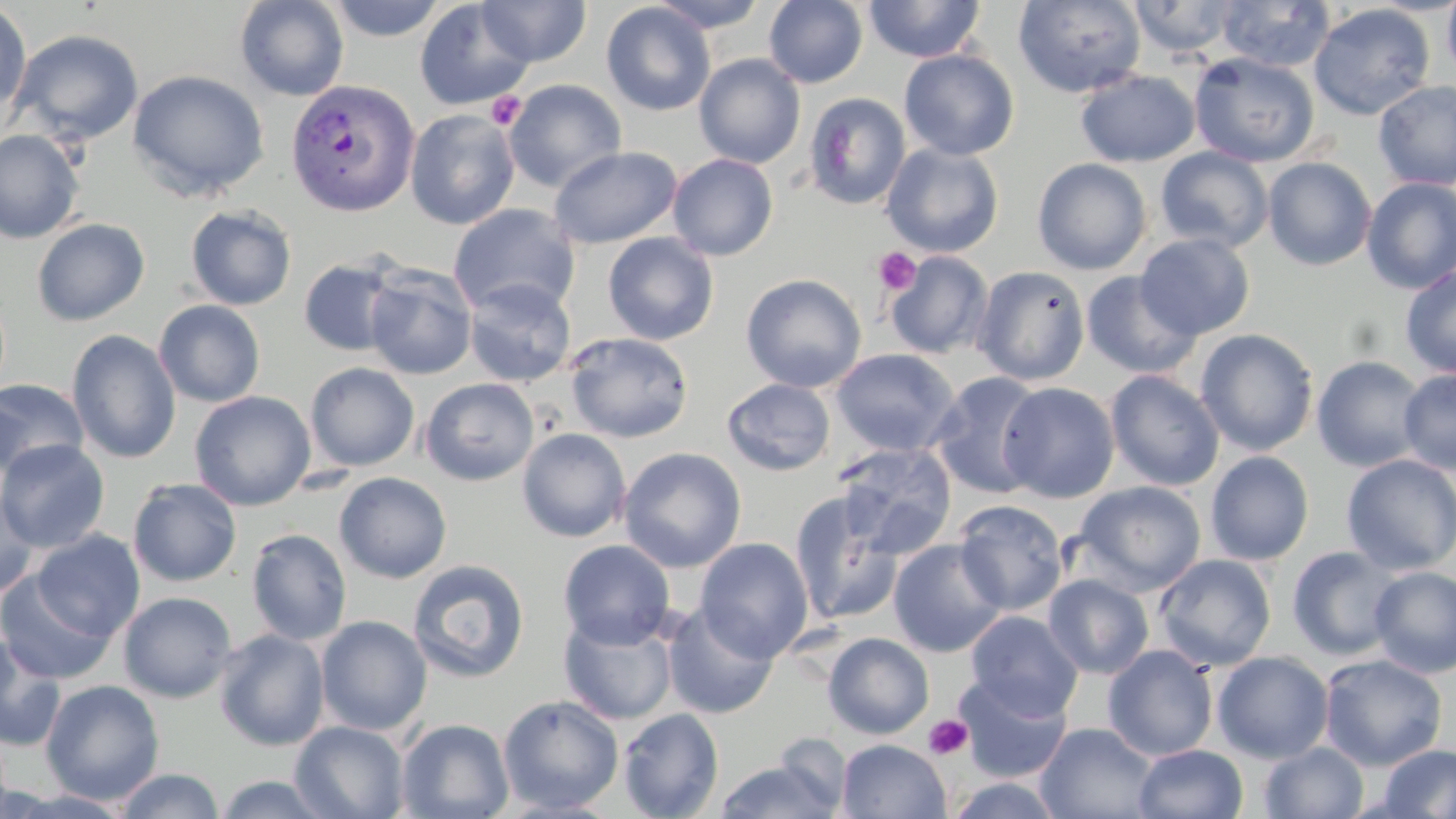 Approximate bounding boxes as named x1/y1/x2/y2 corners in pixels. Uninfected red blood cell locations: (x1=235, y1=0, x2=349, y2=101), (x1=326, y1=0, x2=448, y2=41), (x1=648, y1=0, x2=770, y2=33), (x1=763, y1=0, x2=868, y2=88), (x1=864, y1=0, x2=985, y2=63), (x1=1013, y1=0, x2=1146, y2=98), (x1=1128, y1=0, x2=1242, y2=57), (x1=1441, y1=0, x2=1456, y2=83), (x1=414, y1=1, x2=534, y2=110), (x1=476, y1=1, x2=591, y2=67), (x1=1214, y1=1, x2=1336, y2=72), (x1=601, y1=2, x2=716, y2=116), (x1=0, y1=3, x2=32, y2=119), (x1=1308, y1=4, x2=1435, y2=121), (x1=10, y1=29, x2=144, y2=146), (x1=899, y1=49, x2=1020, y2=160), (x1=1189, y1=52, x2=1320, y2=168), (x1=694, y1=53, x2=806, y2=169), (x1=127, y1=68, x2=270, y2=201), (x1=1075, y1=69, x2=1200, y2=167), (x1=503, y1=79, x2=627, y2=191), (x1=1373, y1=80, x2=1456, y2=190), (x1=804, y1=93, x2=912, y2=210), (x1=405, y1=108, x2=520, y2=230), (x1=0, y1=129, x2=85, y2=244), (x1=880, y1=143, x2=1005, y2=257), (x1=550, y1=145, x2=683, y2=249), (x1=1155, y1=146, x2=1274, y2=253), (x1=668, y1=153, x2=779, y2=260), (x1=1032, y1=157, x2=1152, y2=275), (x1=1262, y1=157, x2=1377, y2=270), (x1=1360, y1=177, x2=1456, y2=294), (x1=448, y1=203, x2=580, y2=318), (x1=185, y1=205, x2=297, y2=310), (x1=31, y1=218, x2=150, y2=326), (x1=602, y1=232, x2=719, y2=345), (x1=1135, y1=232, x2=1256, y2=340), (x1=884, y1=250, x2=993, y2=359), (x1=298, y1=258, x2=403, y2=356), (x1=1400, y1=264, x2=1456, y2=378), (x1=364, y1=265, x2=477, y2=379), (x1=973, y1=265, x2=1090, y2=385), (x1=1081, y1=271, x2=1203, y2=379), (x1=741, y1=273, x2=867, y2=393), (x1=462, y1=278, x2=576, y2=387), (x1=154, y1=299, x2=266, y2=407), (x1=1195, y1=328, x2=1319, y2=456), (x1=67, y1=330, x2=181, y2=464), (x1=564, y1=332, x2=694, y2=443), (x1=831, y1=348, x2=959, y2=457), (x1=1311, y1=355, x2=1428, y2=472), (x1=305, y1=362, x2=420, y2=471), (x1=1398, y1=368, x2=1456, y2=474), (x1=1105, y1=370, x2=1224, y2=491), (x1=929, y1=372, x2=1047, y2=499), (x1=722, y1=377, x2=836, y2=476), (x1=0, y1=378, x2=89, y2=479), (x1=420, y1=378, x2=539, y2=486), (x1=998, y1=381, x2=1120, y2=503), (x1=190, y1=391, x2=316, y2=511), (x1=517, y1=427, x2=631, y2=543), (x1=0, y1=439, x2=110, y2=553), (x1=833, y1=442, x2=957, y2=560), (x1=618, y1=447, x2=747, y2=573), (x1=1205, y1=451, x2=1314, y2=564), (x1=1341, y1=454, x2=1456, y2=575), (x1=334, y1=472, x2=452, y2=583), (x1=128, y1=478, x2=242, y2=587), (x1=1074, y1=480, x2=1207, y2=596), (x1=0, y1=487, x2=41, y2=599), (x1=789, y1=491, x2=903, y2=626), (x1=952, y1=499, x2=1068, y2=615), (x1=246, y1=528, x2=351, y2=645), (x1=30, y1=530, x2=145, y2=641), (x1=695, y1=537, x2=813, y2=662), (x1=888, y1=539, x2=1008, y2=657), (x1=558, y1=540, x2=676, y2=649), (x1=1286, y1=545, x2=1405, y2=661), (x1=1154, y1=554, x2=1276, y2=671), (x1=407, y1=560, x2=530, y2=684), (x1=1368, y1=566, x2=1456, y2=679), (x1=0, y1=572, x2=117, y2=685), (x1=1043, y1=574, x2=1154, y2=679), (x1=118, y1=591, x2=238, y2=702), (x1=662, y1=604, x2=779, y2=719), (x1=966, y1=610, x2=1084, y2=721), (x1=558, y1=613, x2=679, y2=726), (x1=316, y1=615, x2=432, y2=736), (x1=213, y1=629, x2=330, y2=751), (x1=822, y1=632, x2=935, y2=740), (x1=0, y1=634, x2=66, y2=751), (x1=1103, y1=644, x2=1219, y2=761), (x1=1212, y1=651, x2=1334, y2=763), (x1=1319, y1=653, x2=1448, y2=771), (x1=953, y1=673, x2=1072, y2=783), (x1=41, y1=679, x2=165, y2=804), (x1=497, y1=694, x2=624, y2=814), (x1=617, y1=708, x2=724, y2=819), (x1=396, y1=718, x2=515, y2=819), (x1=290, y1=720, x2=411, y2=818), (x1=1036, y1=722, x2=1159, y2=818), (x1=769, y1=738, x2=860, y2=813), (x1=836, y1=739, x2=951, y2=819), (x1=1259, y1=741, x2=1369, y2=819), (x1=1376, y1=743, x2=1456, y2=819), (x1=1133, y1=744, x2=1248, y2=819), (x1=715, y1=759, x2=843, y2=819), (x1=113, y1=768, x2=225, y2=819), (x1=213, y1=774, x2=334, y2=818), (x1=943, y1=776, x2=1068, y2=819). Plasmodium vivax-infected red blood cell locations: (x1=284, y1=78, x2=420, y2=216). Platelet locations: (x1=487, y1=91, x2=526, y2=130), (x1=872, y1=247, x2=921, y2=296), (x1=923, y1=714, x2=974, y2=760). Slide-level diagnosis: Plasmodium vivax. One field of a larger specimen. Optical microscopy. Image is 1456×819 pixels. May-Grünwald-Giemsa stain. 1000x magnification. Thin blood film.